Assess this cell for malaria.
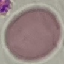
It is uninfected.

stain: Giemsa
capture: smartphone through the microscope eyepiece
image_type: cell patch, automatically extracted from a larger field of view and resized to 64 × 64 pixels
preparation: thin blood film